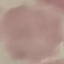 Malaria status: uninfected. Giemsa stain. Photographed with a smartphone camera at the microscope eyepiece. Thin blood smear. Automatically extracted cell patch, resized to 64 × 64 pixels.